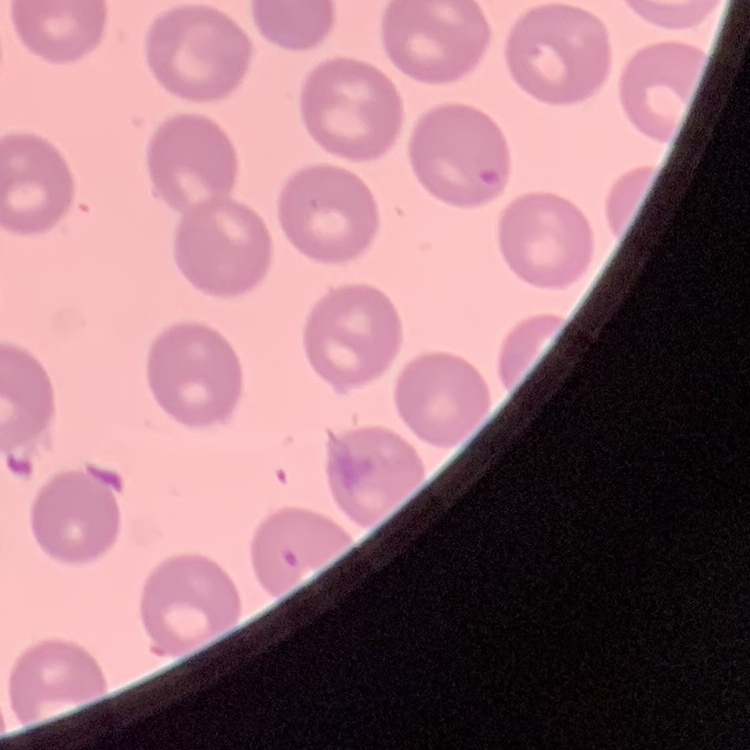

Summary:
  - Erythrocyte morphology: no rouleaux formation
  - Image type: square crop of a larger photomicrograph
  - Preparation: thin blood smear
  - Stain: Field's or Giemsa